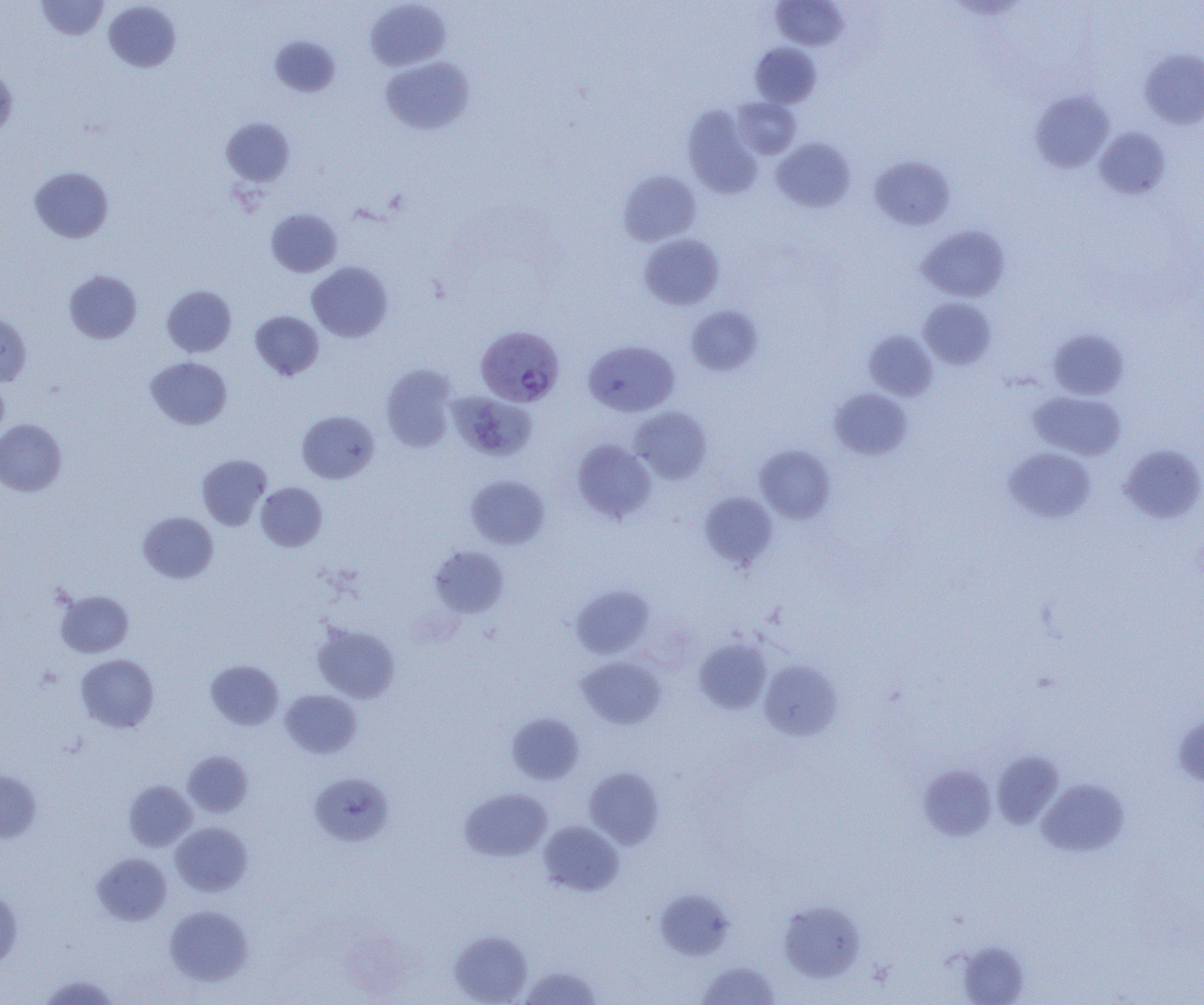
Summary:
  - Coordinate format: approximate bounding boxes as (x1,y1)-(x2,y2) corner pairs in pixels
  - Plasmodium vivax-infected red blood cell locations: (476,325)-(565,407)
  - Uninfected red blood cell locations: (36,1)-(109,40), (103,1)-(181,72), (365,1)-(451,70), (771,1)-(848,50), (269,35)-(341,97), (750,42)-(821,108), (1139,48)-(1204,129), (380,56)-(475,135), (0,65)-(18,139), (1030,89)-(1114,173), (732,97)-(801,159), (683,105)-(763,199), (221,118)-(295,187), (1095,126)-(1171,200), (771,138)-(856,212), (868,155)-(955,231), (29,166)-(114,243), (618,170)-(701,245), (266,208)-(342,277), (917,225)-(1010,302), (639,233)-(725,310), (306,261)-(393,341), (63,270)-(142,344), (162,285)-(236,357), (919,298)-(996,369), (686,305)-(763,376), (250,310)-(324,381), (0,313)-(31,387), (1047,328)-(1129,399), (864,329)-(938,401), (583,340)-(679,416), (145,356)-(232,429), (380,364)-(458,452), (0,378)-(9,445), (829,388)-(912,460), (450,391)-(537,462), (1028,391)-(1126,460), (630,406)-(713,484), (297,410)-(380,483), (0,419)-(67,496), (572,439)-(657,524), (1119,443)-(1204,523), (755,445)-(835,523), (1004,447)-(1096,522), (196,454)-(271,531), (466,475)-(550,549), (255,482)-(327,552), (699,492)-(778,570), (138,511)-(218,583), (430,546)-(510,617), (571,585)-(654,658), (55,590)-(134,657), (312,621)-(400,703), (693,637)-(771,715), (76,654)-(159,733), (577,655)-(666,729), (206,660)-(284,730), (759,660)-(842,741), (280,689)-(362,758), (507,713)-(585,784), (1173,714)-(1204,787), (992,750)-(1064,829), (183,751)-(253,817), (919,764)-(997,841), (584,767)-(664,849), (0,770)-(41,843), (309,772)-(395,845), (1037,778)-(1128,857), (124,780)-(196,851), (461,788)-(553,861), (538,820)-(624,896), (170,821)-(252,896), (92,853)-(172,925), (0,887)-(22,970), (656,889)-(735,960), (779,900)-(865,982), (164,905)-(253,986), (449,930)-(532,1004), (956,941)-(1030,1005), (696,961)-(781,1004), (519,966)-(602,1005), (39,974)-(120,1004)
  - Slide-level diagnosis: Plasmodium vivax
  - Image size: 1204×1005 pixels
  - Modality: light microscopy
  - Magnification: 1000x
  - Field of view: single
  - Preparation: thin blood smear